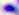

400x magnification. Micrograph. Toxoplasma gondii is shown.